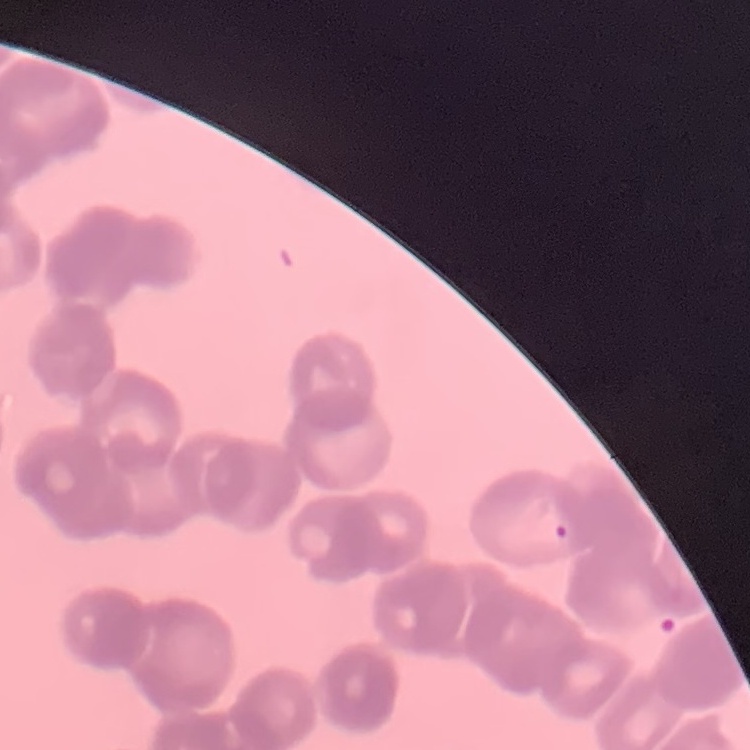

red_blood_cell_morphology: rouleaux formation
stain: Field's or Giemsa
image_type: one tile cut from a larger photomicrograph
preparation: thin blood film